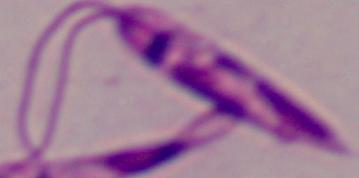

magnification = 1000x
modality = micrograph
identification = Leishmania